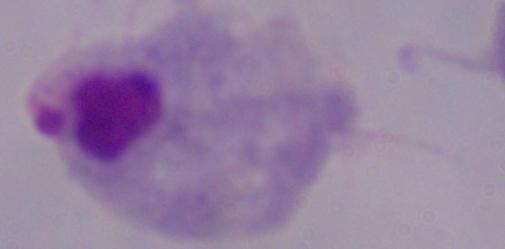
1000x magnification. Micrograph. A trichomonad is seen.